Mark where platelets are.
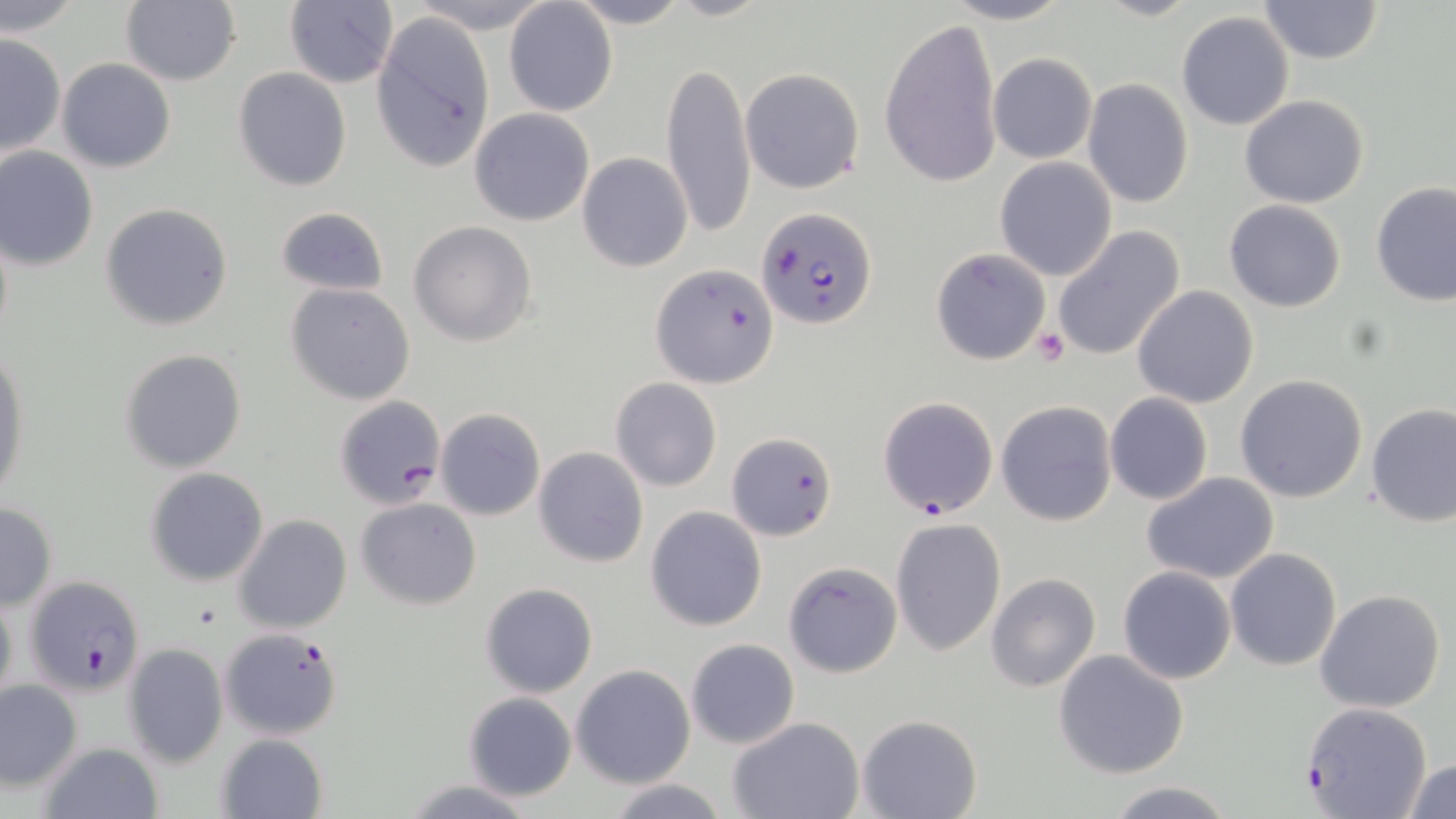
Approximate bounding boxes as (x1,y1)-(x2,y2) corner pairs in pixels.
Platelets: (1032,329)-(1068,366).

Uninfected red blood cell locations: (2,0)-(81,37), (120,0)-(240,87), (406,0)-(553,33), (566,0)-(691,30), (666,0)-(771,22), (940,0)-(1077,25), (1256,0)-(1384,66), (504,1)-(617,118), (283,2)-(399,88), (369,7)-(496,176), (1176,11)-(1294,131), (879,17)-(1003,189), (0,33)-(67,159), (986,52)-(1098,164), (57,58)-(177,172), (660,62)-(755,241), (739,66)-(867,194), (233,67)-(351,192), (1083,78)-(1194,209), (1239,95)-(1368,207), (468,108)-(596,227), (0,146)-(99,271), (578,152)-(693,273), (995,157)-(1119,282), (1370,181)-(1455,306), (1224,199)-(1346,312), (100,202)-(234,330), (275,205)-(389,298), (408,221)-(538,347), (1052,227)-(1186,363), (930,247)-(1050,366), (653,264)-(778,389), (287,283)-(415,405), (1132,285)-(1259,409), (0,345)-(30,500), (119,347)-(246,473), (1234,373)-(1369,504), (611,377)-(722,491), (1105,392)-(1214,506), (996,400)-(1118,526), (1365,402)-(1455,527), (435,408)-(545,521), (725,431)-(837,542), (533,446)-(649,568), (144,467)-(269,587), (1141,473)-(1280,584), (354,498)-(482,609), (0,502)-(57,610), (645,506)-(767,632), (232,514)-(353,635), (889,517)-(1007,656), (1225,548)-(1342,670), (783,560)-(903,679), (1117,565)-(1237,684), (986,572)-(1101,692), (479,581)-(598,698), (0,586)-(17,711), (1315,588)-(1446,713), (685,638)-(799,750), (123,643)-(228,766), (1052,649)-(1190,778), (571,664)-(696,788), (1,679)-(83,792), (461,691)-(577,803), (857,713)-(982,818), (726,716)-(864,819), (215,732)-(328,818), (35,741)-(163,819), (1403,757)-(1456,818), (400,778)-(536,818), (605,778)-(731,818), (1104,780)-(1237,818). Plasmodium falciparum-infected red blood cell locations: (758,207)-(877,330), (333,395)-(448,510), (877,396)-(995,519), (24,574)-(149,697), (219,627)-(344,739), (1302,701)-(1432,819). Slide-level diagnosis: Plasmodium falciparum. Thin blood smear. Image is 1456×819 pixels. Single field of view. Light microscopy. 1000x magnification. May-Grünwald-Giemsa-stained preparation.